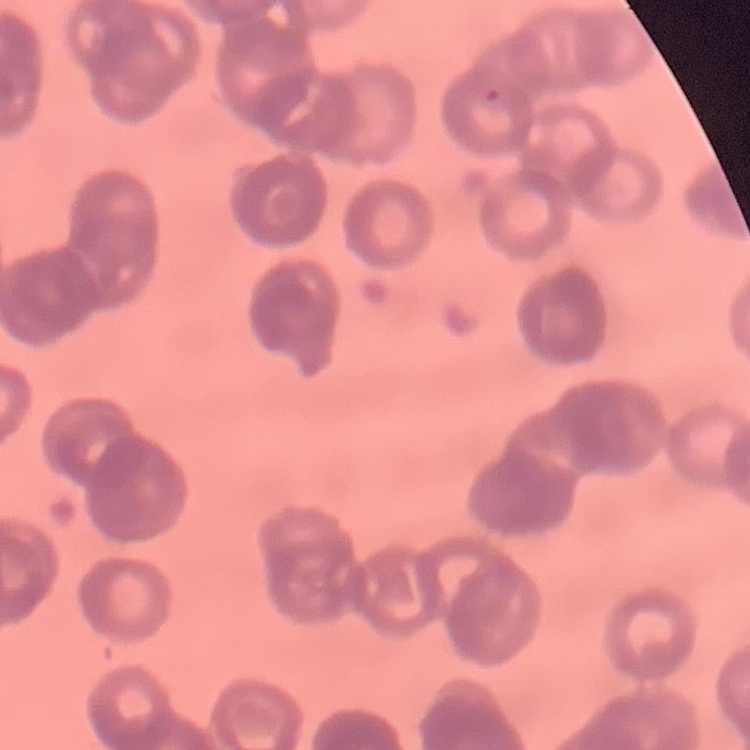
Summary:
  - Red blood cell morphology: rouleaux formation
  - Image type: square crop of a larger photomicrograph
  - Preparation: thin blood smear
  - Stain: Field's or Giemsa